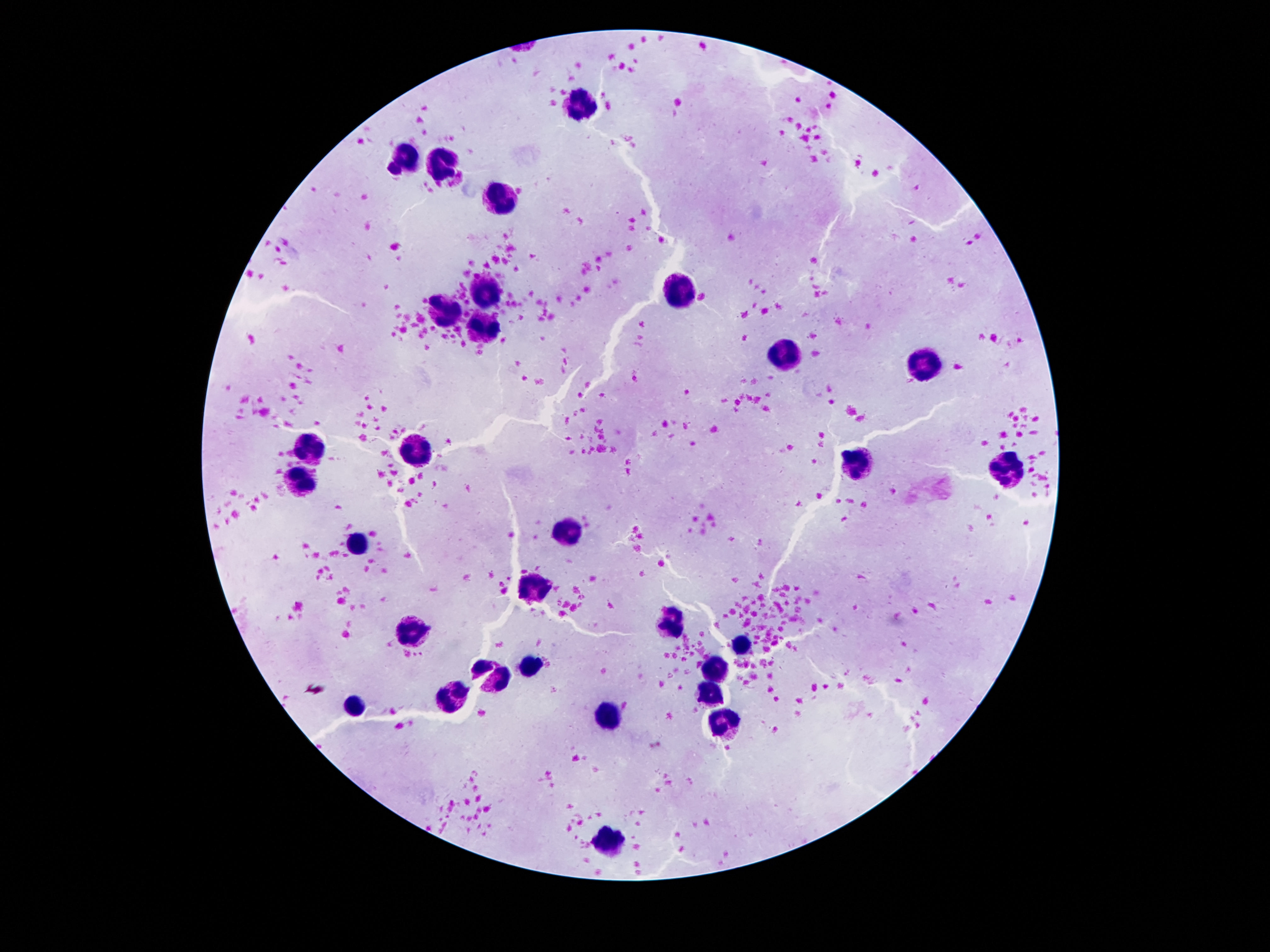
Approximate object centers, in pixels from the top-left corner. Leukocyte locations: (x=580, y=106), (x=402, y=160), (x=447, y=168), (x=501, y=199), (x=486, y=289), (x=673, y=291), (x=445, y=310), (x=481, y=325), (x=785, y=356), (x=930, y=363), (x=309, y=444), (x=412, y=453), (x=1005, y=461), (x=858, y=466), (x=302, y=479), (x=567, y=533), (x=361, y=543), (x=529, y=587), (x=669, y=623), (x=408, y=632), (x=742, y=648), (x=533, y=664), (x=712, y=673), (x=451, y=699), (x=708, y=701), (x=354, y=703), (x=608, y=716), (x=731, y=724), (x=606, y=836). Thick blood film. Photographed through the microscope eyepiece with a smartphone camera. One field from this slide. 100x magnification. Patient malaria status: uninfected. Image is 1270×952 pixels. Giemsa stain.